Identify the cell.
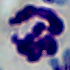
A leukocyte.

magnification = 1000x
modality = micrograph